Point out every malaria parasite and every leukocyte.
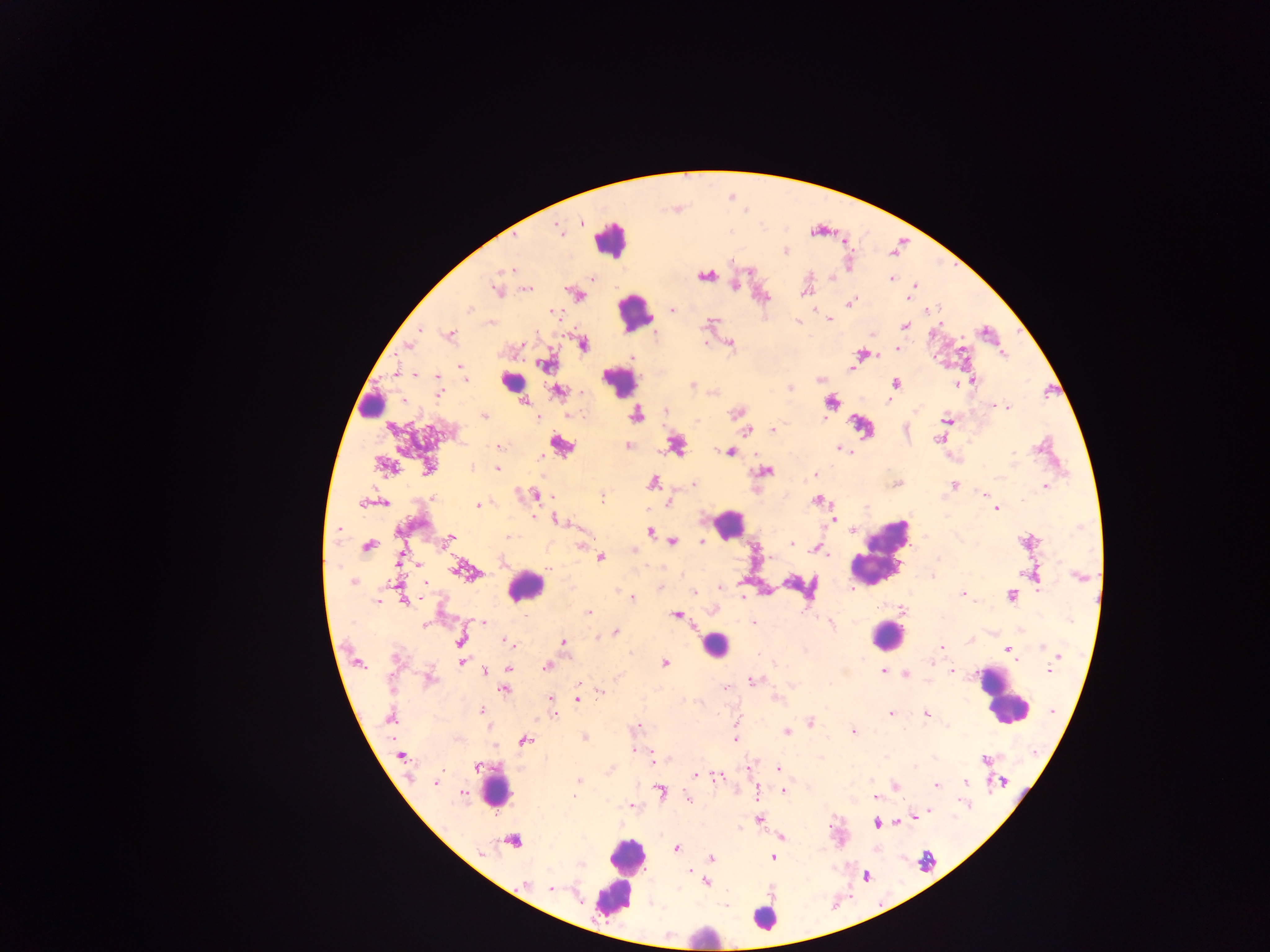

Approximate centers as x y in pixels.
Malaria parasites: 581 223; 558 229; 785 251; 503 269; 510 269; 705 276; 591 278; 891 279; 734 285; 914 286; 528 289; 495 290; 805 292; 581 296; 909 298; 849 303; 469 309; 673 310; 552 311; 829 319; 797 320; 905 326; 419 330; 450 334; 730 342; 705 343; 522 344; 584 344; 409 346; 898 350; 862 354; 1004 355; 633 357; 546 365; 852 368; 396 373; 415 374; 437 378; 465 379; 972 380; 895 383; 957 384; 693 386; 790 388; 558 392; 439 393; 888 401; 524 402; 998 405; 1008 407; 665 410; 737 413; 484 416; 636 416; 538 418; 823 419; 946 420; 773 429; 748 431; 938 439; 499 446; 628 446; 676 446; 839 448; 730 452; 472 466; 385 467; 428 467; 497 469; 764 471; 815 475; 653 483; 694 484; 896 484; 954 486; 1046 486; 983 493; 536 495; 602 497; 819 500; 363 503; 384 503; 669 503; 477 506; 997 509; 533 517; 555 520; 834 520; 337 529; 852 530; 650 532; 508 537; 451 538; 672 542; 702 542; 1026 542; 791 544; 581 545; 368 546; 817 549; 827 555; 771 557; 601 558; 399 561; 464 571; 1079 576; 353 583; 390 584; 424 584; 721 587; 694 592; 963 593; 1011 595; 742 597; 631 598; 403 600; 377 602; 902 610; 589 612; 676 615; 526 616; 483 623; 753 623; 830 623; 422 625; 615 632; 460 641; 507 641; 563 641; 971 641; 1043 646; 942 647; 1007 650; 1058 656; 395 658; 1014 659; 358 663; 463 663; 664 663; 931 663; 547 666; 510 669; 883 671; 951 671; 1049 671; 484 672; 906 674; 431 679; 751 681; 579 683; 725 688; 504 690; 600 691; 551 699; 578 699; 481 710; 1052 711; 891 713; 926 714; 390 717; 810 722; 635 727; 787 732; 853 732; 584 737; 735 739; 523 740; 632 750; 401 755; 984 759; 653 762; 476 766; 778 769; 696 775; 719 777; 578 780; 965 782; 435 783; 1004 783; 937 785; 896 786; 758 791; 784 791; 463 792; 660 792; 574 796; 874 796; 688 798; 963 804; 630 806; 930 811; 915 818; 759 820; 897 822; 876 824; 783 837; 512 841; 677 848; 773 857; 712 858; 689 871; 706 882; 525 883; 551 889.
Leukocytes: 610 240; 635 311; 619 381; 511 384; 371 401; 560 448; 729 524; 881 551; 526 586; 886 635; 713 645; 1004 697; 495 791; 620 874; 765 917; 703 936.

Image is 1270×952 pixels. Collected in Ghana. One field of view. Mobile-phone photograph taken through the microscope. Thick blood film.